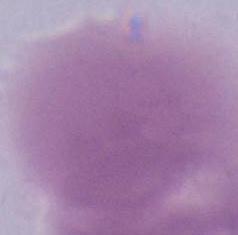

modality = photomicrograph
identification = erythrocyte
magnification = 1000x